Identify the parasite.
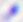

Toxoplasma gondii.

magnification = 400x
modality = photomicrograph